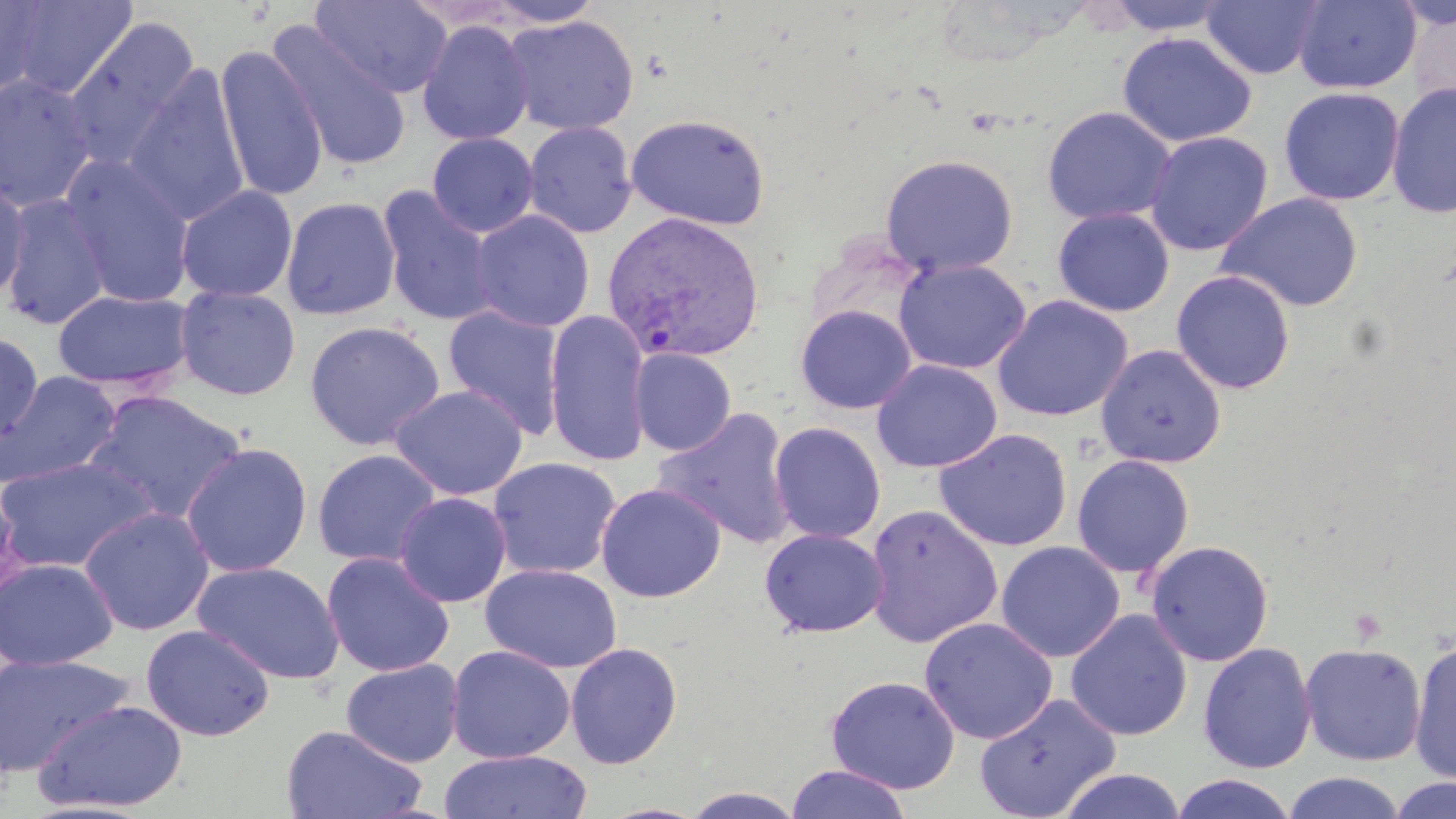 Approximate bounding boxes as named x1/y1/x2/y2 corners in pixels. Plasmodium vivax-infected red blood cell locations: (x1=602, y1=211, x2=767, y2=363). Platelet locations: (x1=1348, y1=607, x2=1388, y2=644). Uninfected red blood cell locations: (x1=6, y1=0, x2=137, y2=100), (x1=310, y1=0, x2=452, y2=98), (x1=484, y1=0, x2=606, y2=27), (x1=1101, y1=0, x2=1234, y2=35), (x1=1201, y1=0, x2=1325, y2=80), (x1=1292, y1=0, x2=1421, y2=93), (x1=0, y1=1, x2=46, y2=98), (x1=503, y1=14, x2=640, y2=136), (x1=62, y1=15, x2=202, y2=172), (x1=416, y1=21, x2=534, y2=146), (x1=267, y1=22, x2=413, y2=170), (x1=1116, y1=31, x2=1257, y2=147), (x1=214, y1=43, x2=328, y2=203), (x1=123, y1=63, x2=250, y2=226), (x1=0, y1=73, x2=99, y2=213), (x1=1386, y1=81, x2=1456, y2=220), (x1=1279, y1=86, x2=1405, y2=206), (x1=1041, y1=106, x2=1177, y2=226), (x1=625, y1=113, x2=770, y2=231), (x1=524, y1=121, x2=638, y2=238), (x1=1144, y1=131, x2=1273, y2=256), (x1=427, y1=132, x2=539, y2=238), (x1=61, y1=153, x2=195, y2=309), (x1=879, y1=153, x2=1019, y2=278), (x1=0, y1=176, x2=31, y2=305), (x1=176, y1=184, x2=298, y2=302), (x1=377, y1=186, x2=499, y2=327), (x1=2, y1=191, x2=112, y2=329), (x1=1215, y1=192, x2=1365, y2=313), (x1=280, y1=195, x2=401, y2=321), (x1=1052, y1=207, x2=1175, y2=317), (x1=470, y1=209, x2=594, y2=332), (x1=894, y1=258, x2=1031, y2=374), (x1=1171, y1=270, x2=1296, y2=395), (x1=174, y1=284, x2=301, y2=401), (x1=52, y1=288, x2=195, y2=392), (x1=992, y1=294, x2=1133, y2=422), (x1=795, y1=304, x2=917, y2=414), (x1=442, y1=305, x2=565, y2=439), (x1=544, y1=309, x2=652, y2=466), (x1=304, y1=320, x2=445, y2=450), (x1=0, y1=332, x2=43, y2=442), (x1=1095, y1=344, x2=1227, y2=468), (x1=630, y1=348, x2=736, y2=456), (x1=871, y1=358, x2=1002, y2=474), (x1=0, y1=371, x2=122, y2=488), (x1=389, y1=384, x2=527, y2=500), (x1=83, y1=390, x2=248, y2=523), (x1=653, y1=407, x2=797, y2=549), (x1=769, y1=421, x2=886, y2=544), (x1=933, y1=428, x2=1073, y2=552), (x1=180, y1=442, x2=313, y2=578), (x1=312, y1=448, x2=443, y2=568), (x1=1071, y1=454, x2=1195, y2=579), (x1=0, y1=456, x2=158, y2=573), (x1=487, y1=457, x2=622, y2=580), (x1=595, y1=482, x2=727, y2=603), (x1=393, y1=491, x2=512, y2=607), (x1=864, y1=503, x2=1003, y2=648), (x1=78, y1=505, x2=215, y2=636), (x1=759, y1=528, x2=889, y2=637), (x1=1145, y1=539, x2=1275, y2=666), (x1=995, y1=541, x2=1125, y2=662), (x1=321, y1=551, x2=455, y2=677), (x1=0, y1=558, x2=119, y2=670), (x1=193, y1=560, x2=344, y2=683), (x1=480, y1=563, x2=623, y2=673), (x1=1065, y1=609, x2=1193, y2=741), (x1=919, y1=617, x2=1057, y2=744), (x1=140, y1=623, x2=275, y2=741), (x1=1409, y1=638, x2=1456, y2=783), (x1=565, y1=642, x2=682, y2=769), (x1=1197, y1=642, x2=1317, y2=774), (x1=1299, y1=642, x2=1426, y2=766), (x1=446, y1=645, x2=576, y2=764), (x1=0, y1=652, x2=134, y2=776), (x1=341, y1=658, x2=465, y2=767), (x1=825, y1=675, x2=960, y2=794), (x1=975, y1=692, x2=1122, y2=819), (x1=33, y1=699, x2=188, y2=812), (x1=796, y1=720, x2=952, y2=813), (x1=280, y1=725, x2=429, y2=818), (x1=438, y1=749, x2=592, y2=819), (x1=784, y1=765, x2=913, y2=819), (x1=1056, y1=768, x2=1188, y2=819), (x1=1283, y1=772, x2=1407, y2=819), (x1=1169, y1=773, x2=1298, y2=818), (x1=1386, y1=777, x2=1456, y2=819), (x1=677, y1=786, x2=809, y2=818). Slide-level diagnosis: Plasmodium vivax. Thin blood smear. Light microscopy. Single field of view. Captured at 1000x magnification. May-Grünwald-Giemsa stain. Image is 1456×819 pixels.